Outline each uninfected red blood cell.
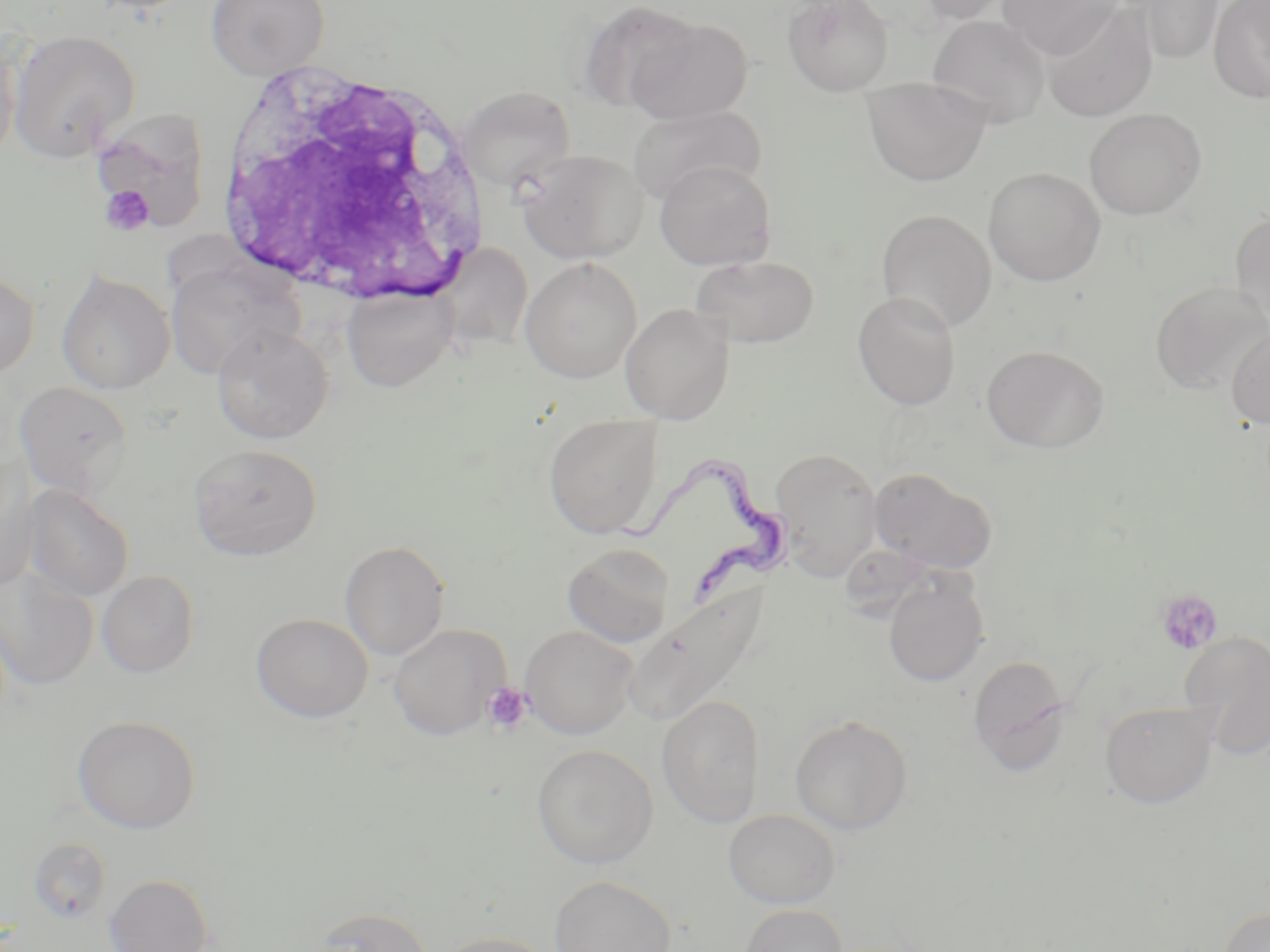

Approximate bounding boxes as (x1,y1)-(x2,y2) corner pairs in pixels.
Uninfected red blood cells: (206,0)-(329,80), (577,0)-(701,113), (782,0)-(895,96), (912,0)-(1018,25), (998,0)-(1123,59), (1125,0)-(1226,65), (1208,0)-(1270,104), (1040,4)-(1159,122), (623,15)-(754,124), (927,15)-(1050,128), (8,30)-(141,161), (861,76)-(991,186), (459,86)-(575,192), (627,104)-(765,206), (90,108)-(210,233), (1084,108)-(1206,220), (515,148)-(648,263), (654,159)-(776,270), (984,167)-(1106,286), (876,210)-(997,332), (1230,212)-(1270,331), (434,244)-(534,353), (690,255)-(819,349), (520,257)-(642,384), (165,258)-(301,378), (0,269)-(39,379), (56,270)-(175,395), (1150,281)-(1269,396), (341,287)-(456,392), (852,291)-(961,411), (619,302)-(734,424), (211,325)-(333,444), (1226,326)-(1270,430), (982,345)-(1109,454), (14,381)-(133,500), (543,414)-(662,539), (188,444)-(323,561), (770,447)-(883,580), (0,458)-(39,591), (869,468)-(997,575), (22,485)-(134,602), (340,540)-(450,660), (563,542)-(675,648), (0,567)-(99,690), (96,570)-(199,678), (882,574)-(989,687), (620,585)-(773,730), (251,613)-(373,723), (388,625)-(509,741), (521,625)-(638,739), (1180,632)-(1270,759), (968,655)-(1071,775), (656,695)-(765,827), (1100,700)-(1218,808), (790,714)-(912,834), (72,716)-(201,834), (532,745)-(658,869), (723,809)-(840,908), (26,837)-(112,925), (104,873)-(215,952), (550,875)-(677,952), (739,903)-(848,952), (308,905)-(435,952), (1219,907)-(1270,952), (428,931)-(560,952).

slide-level diagnosis = Trypanosoma brucei
platelet locations = approximate bounding boxes as (x1,y1)-(x2,y2) corner pairs in pixels: (99,184)-(155,237), (1157,589)-(1223,655), (482,681)-(533,734)
white blood cell locations = approximate bounding boxes as (x1,y1)-(x2,y2) corner pairs in pixels: (211,56)-(494,318)
stain = May-Grünwald-Giemsa
modality = optical microscopy
image size = 1270×952 pixels
preparation = thin blood smear
field of view = one of a larger specimen
Trypanosoma brucei locations = approximate bounding boxes as (x1,y1)-(x2,y2) corner pairs in pixels: (613,447)-(789,610)
magnification = 1000x